Describe the morphology of the erythrocytes.
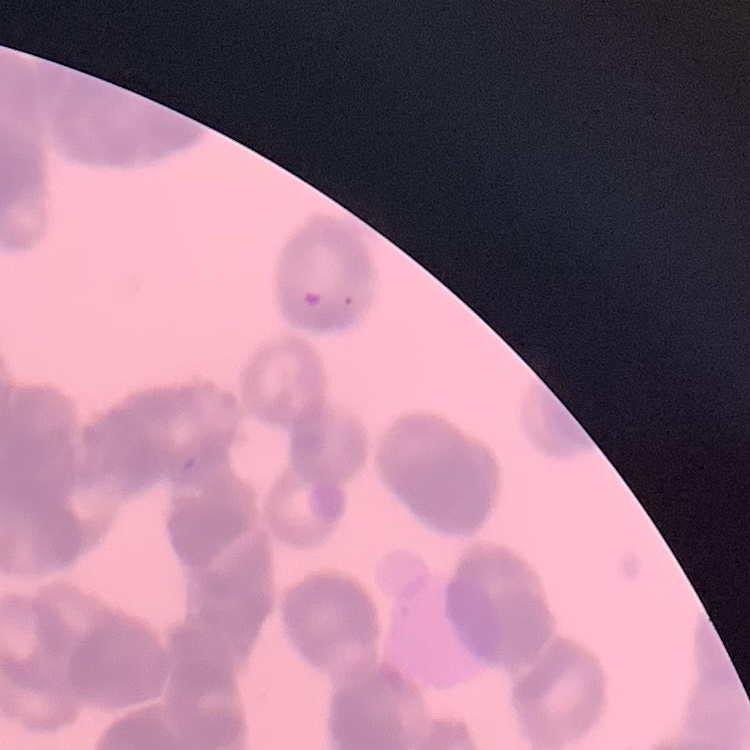
Rouleaux formation.

Summary:
  - Preparation: thin peripheral smear
  - Stain: Field's or Giemsa
  - Image type: one tile cut from a larger photomicrograph